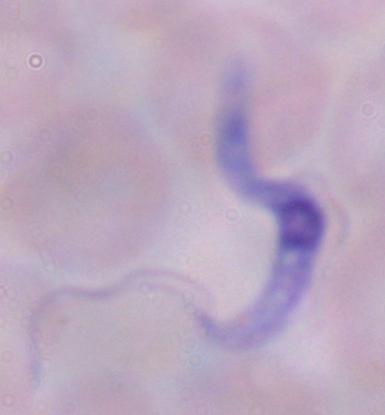
{
  "modality": "photomicrograph",
  "magnification": "1000x",
  "identification": "trypanosome"
}